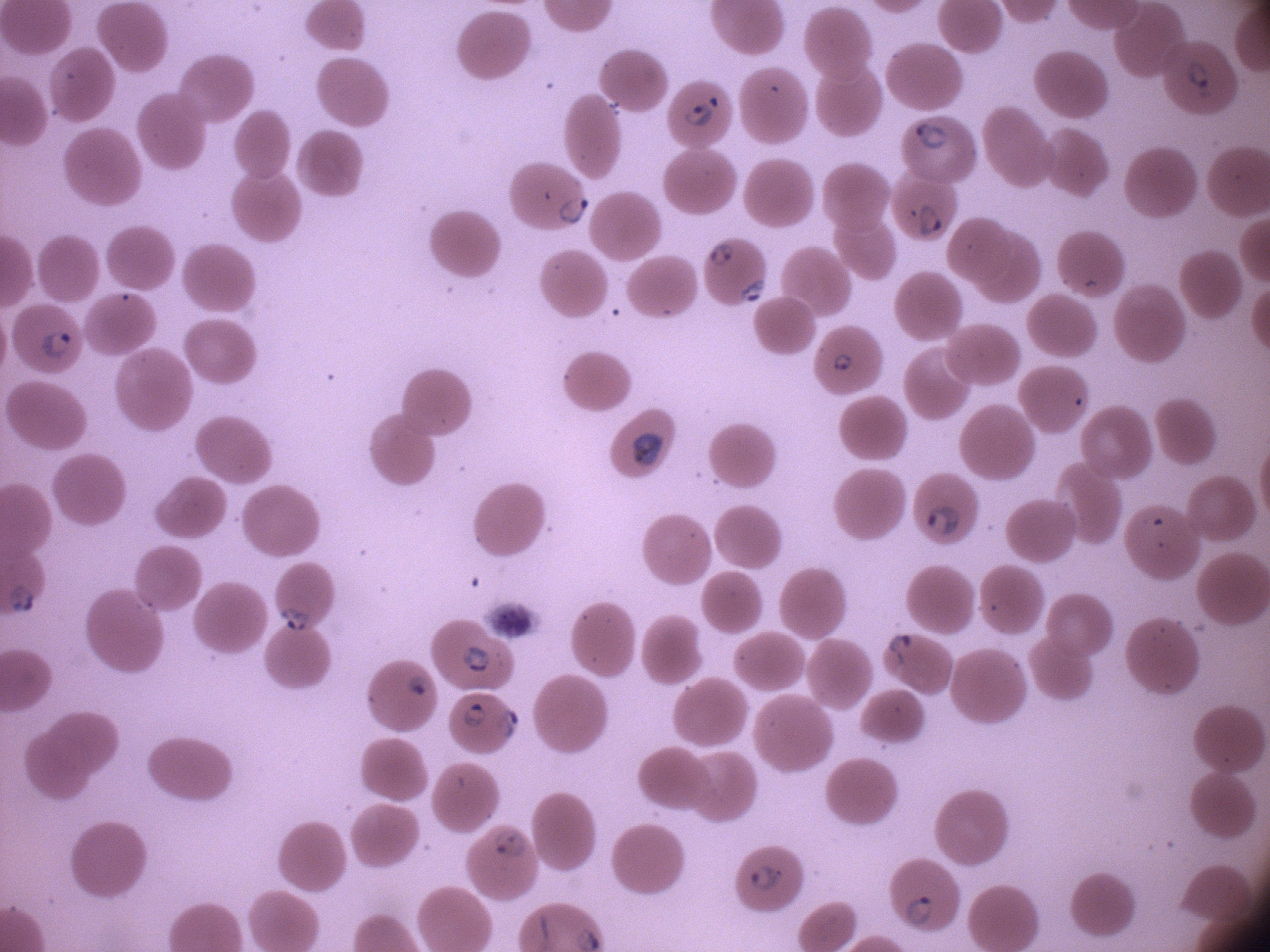

Approximate bounding boxes as (x1, y1, x2, y2) in pixels, from the source annotation, which is not necessarily exhaustive.
Summary:
  - Ring form locations: (1175, 46, 1221, 101), (678, 89, 728, 133), (904, 112, 955, 157), (550, 187, 595, 227), (906, 194, 948, 245), (700, 235, 742, 270), (733, 272, 773, 307), (26, 317, 76, 364), (828, 342, 857, 379), (913, 489, 971, 545), (272, 596, 313, 635), (877, 622, 922, 671), (447, 636, 500, 689), (400, 663, 434, 705), (458, 699, 489, 735), (492, 701, 528, 750), (487, 821, 530, 868), (739, 850, 791, 896), (899, 886, 947, 928)
  - Microscope: Leica DM2000 with built-in camera
  - Field of view: single
  - Stain: Giemsa
  - Magnification: 100x
  - Species: Plasmodium falciparum
  - Image size: 1270×952 pixels
  - Preparation: thin blood smear